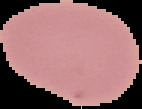

image_size: 142×109 pixels
preparation: thin blood smear
result: negative for Plasmodium parasites
image_type: segmented cell region with the area outside set to black